Point out each leukocyte.
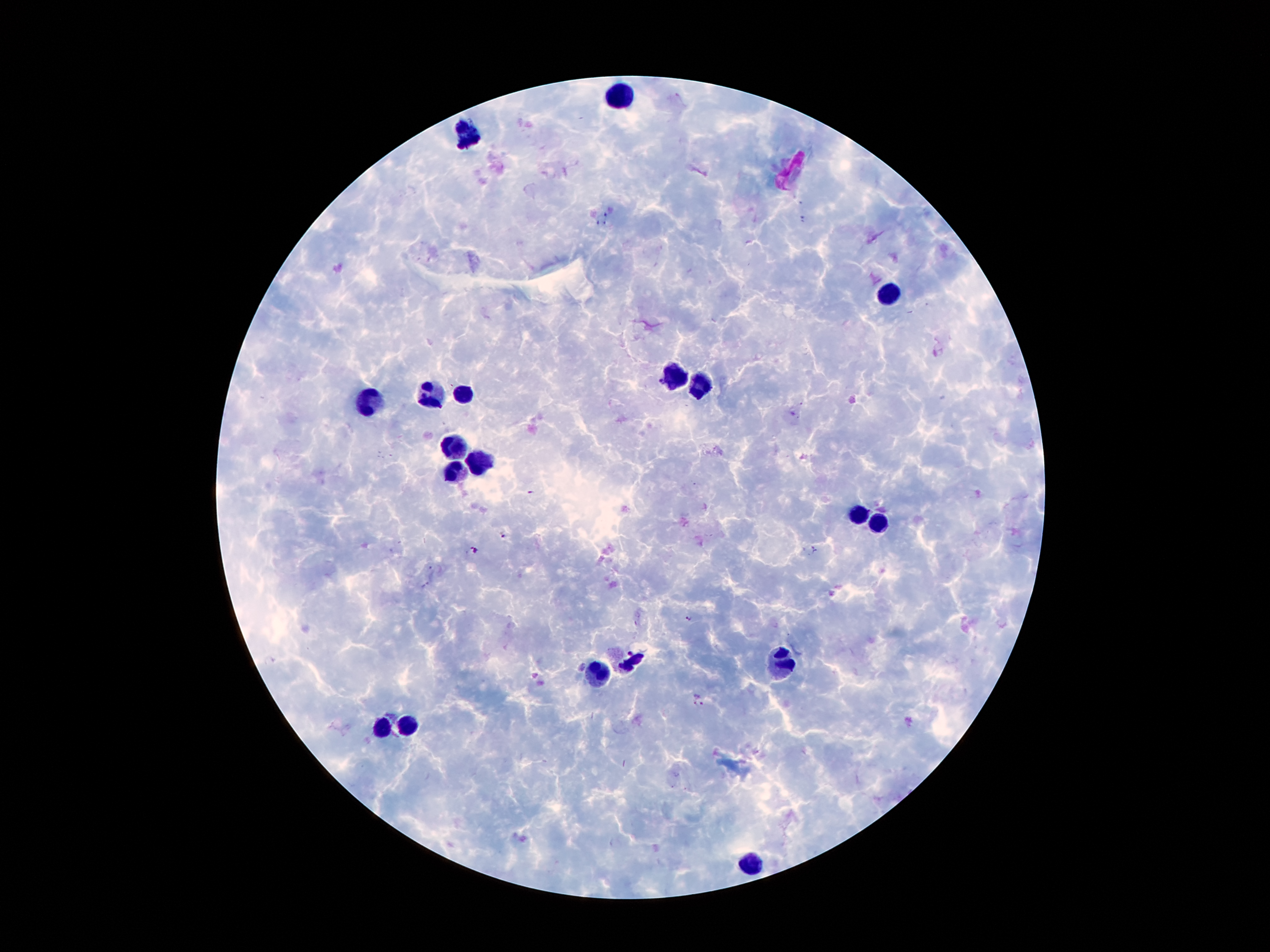

Approximate centers as (x, y) in pixels.
Leukocytes: (618, 95), (468, 136), (892, 291), (675, 375), (704, 384), (463, 393), (429, 397), (365, 402), (452, 443), (484, 459), (452, 470), (858, 511), (877, 522), (634, 657), (783, 664), (597, 670), (384, 725), (407, 725), (752, 863).

Summary:
  - Plasmodium parasite locations: (531, 492), (505, 535), (474, 550), (689, 619), (698, 700)
  - Magnification: 100x
  - Patient malaria status: positive for Plasmodium falciparum
  - Capture: smartphone camera through the microscope eyepiece
  - Preparation: thick blood film
  - Stain: Giemsa
  - Image size: 1270×952 pixels
  - Field of view: single